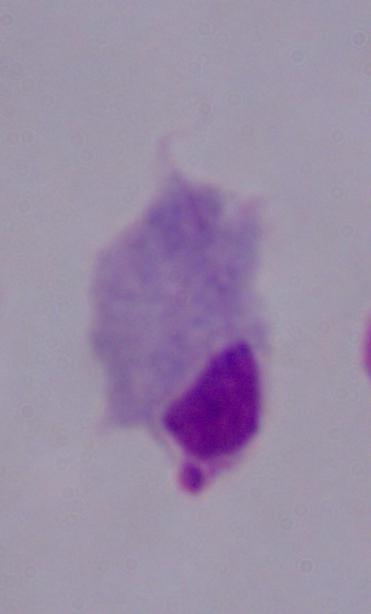

1000x magnification. Photomicrograph. A trichomonad is seen.